Describe the morphology of the erythrocytes.
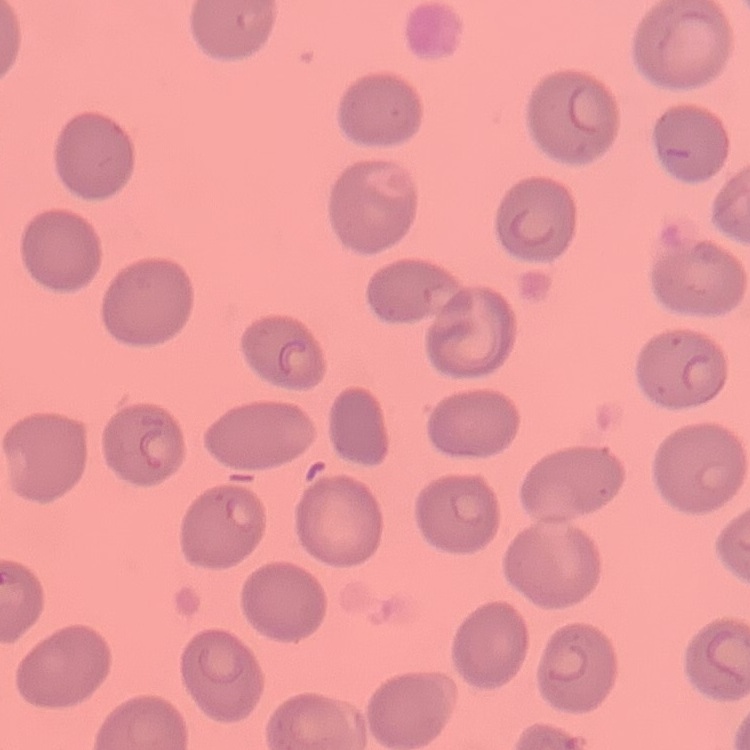
No rouleaux formation.

One tile cut from a larger photomicrograph. Field's or Giemsa stain. Thin blood film.